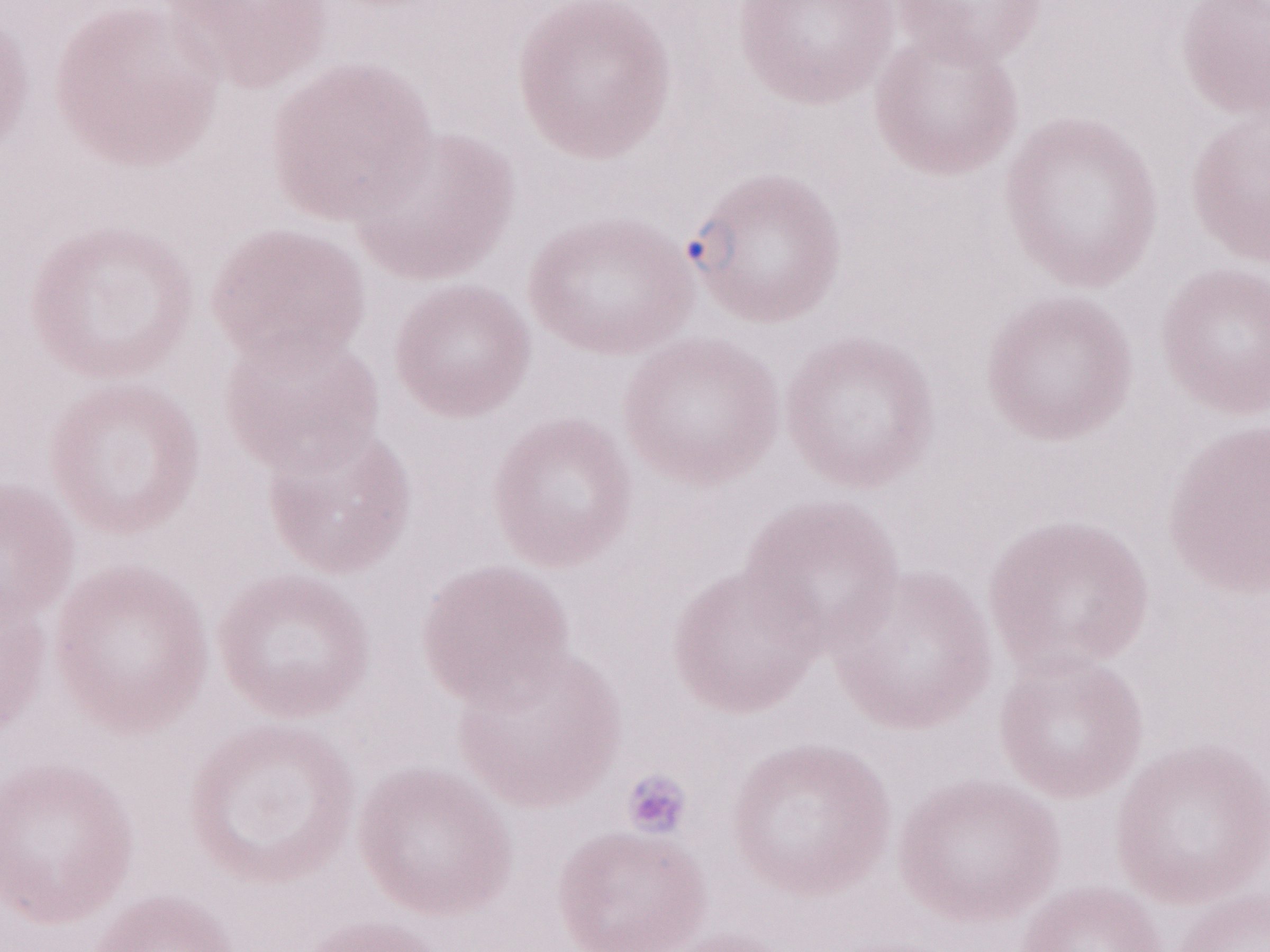
Thin blood smear. 1,000x magnification. May-Grünwald-Giemsa stain. Image is 1270×952 pixels. Malaria diagnosis (patient-level): positive. Olympus BX43 microscope, Olympus DP73 camera. Single field of view.